Locate every Plasmodium parasite.
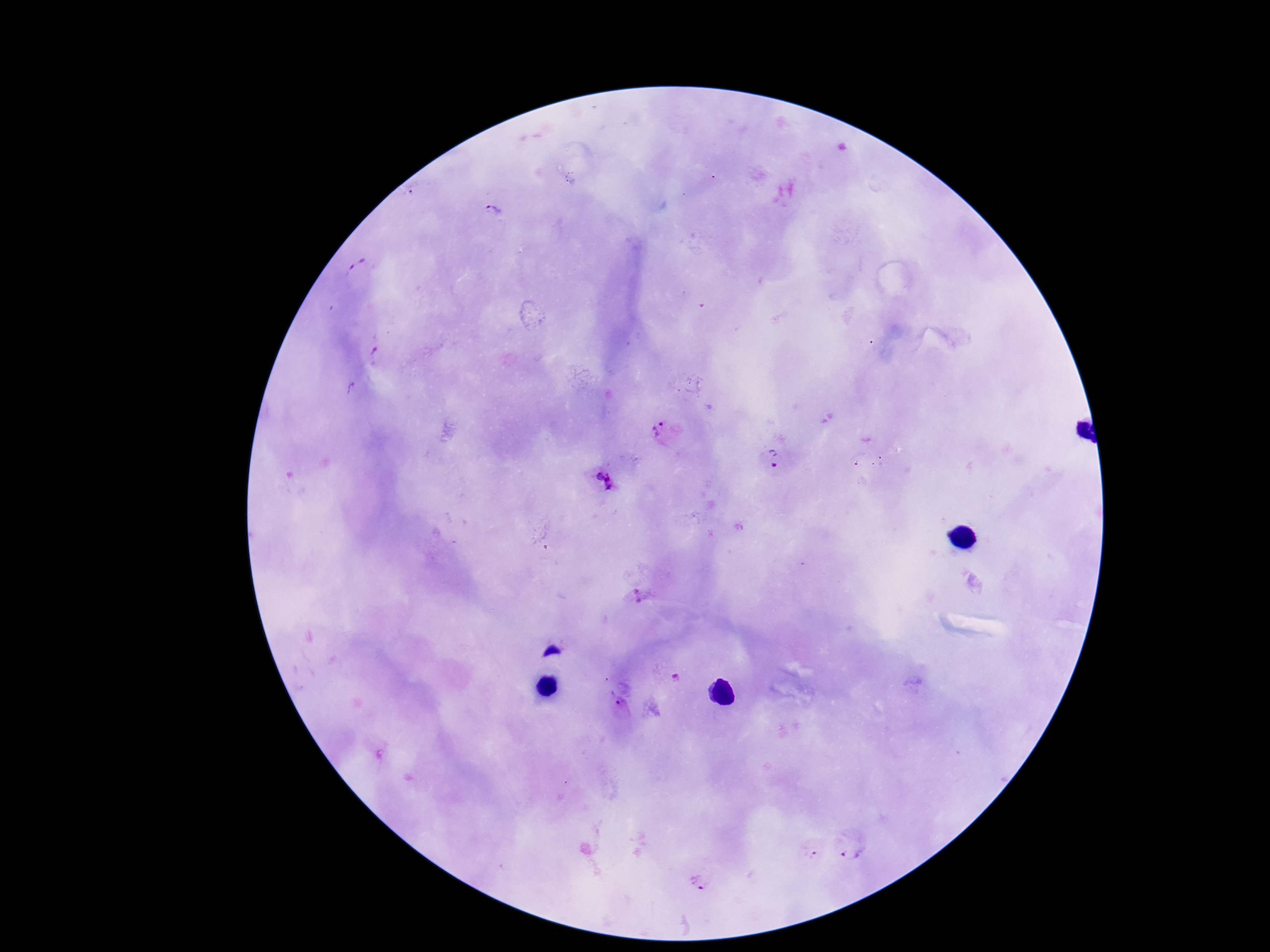
Approximate centers as {x, y} in pixels.
Plasmodium parasites: {495, 210}, {359, 269}, {374, 353}, {663, 432}, {774, 457}, {601, 484}, {637, 596}, {677, 678}, {619, 706}, {850, 850}, {699, 885}.

preparation = thick blood smear
capture = smartphone camera through the microscope eyepiece
patient malaria status = infected
stain = Giemsa
image size = 1270×952 pixels
field of view = single
magnification = 100x